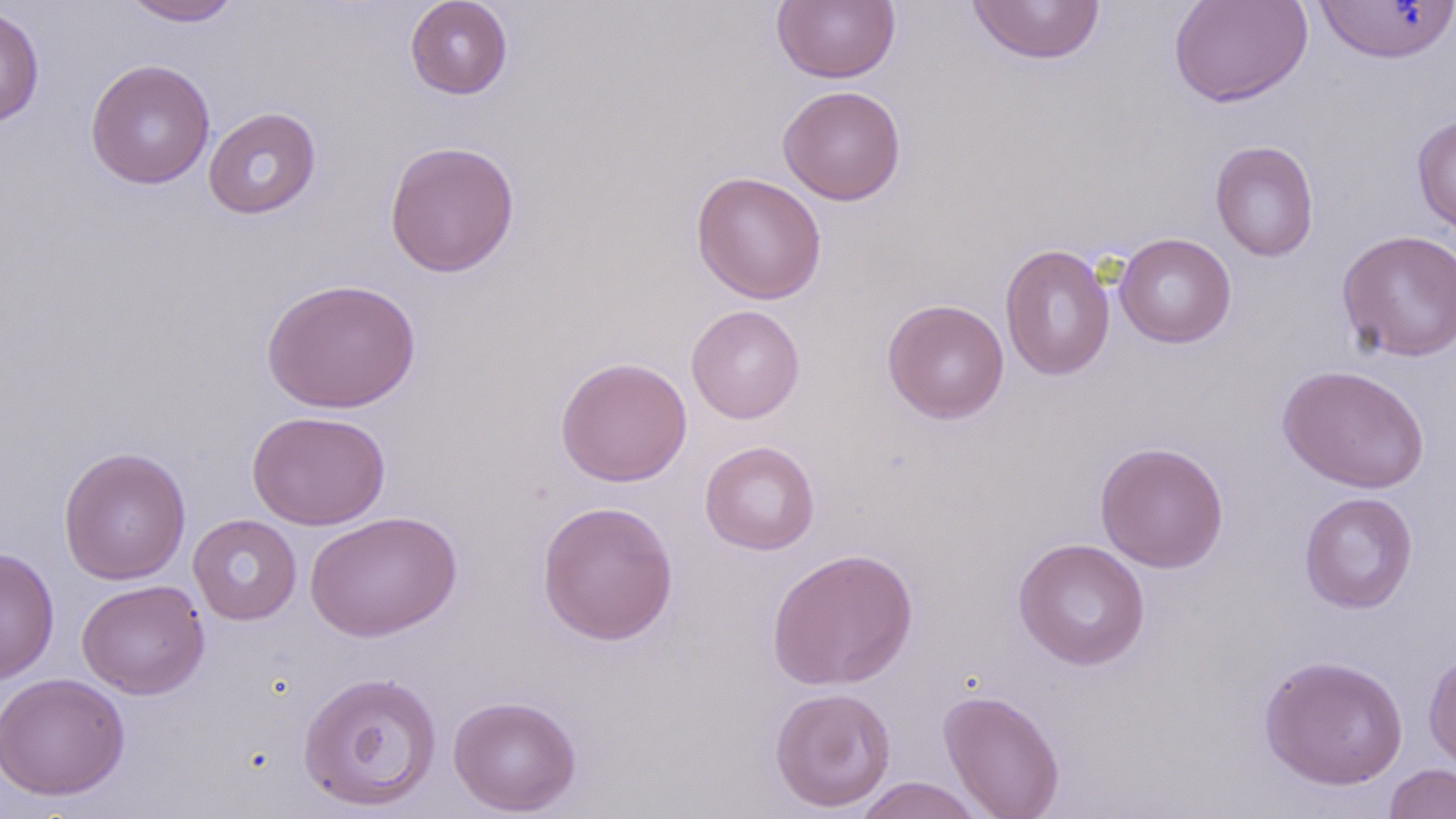 Approximate bounding boxes as (x1,y1)-(x2,y2) corner pairs in pixels. Uninfected red blood cell locations: (120,0)-(244,26), (405,0)-(513,99), (773,0)-(900,84), (1169,0)-(1312,108), (965,1)-(1106,65), (1311,1)-(1456,64), (0,6)-(45,128), (85,59)-(216,189), (778,85)-(907,205), (203,106)-(322,219), (1411,114)-(1456,238), (384,140)-(520,277), (1210,141)-(1320,262), (691,171)-(828,304), (1338,229)-(1456,362), (1115,232)-(1237,348), (999,243)-(1116,381), (261,277)-(421,413), (882,299)-(1009,423), (686,304)-(805,424), (555,356)-(693,487), (1277,364)-(1430,493), (247,410)-(390,531), (700,440)-(820,555), (1095,441)-(1229,573), (58,446)-(191,584), (1299,492)-(1419,613), (537,500)-(678,646), (304,510)-(462,642), (188,514)-(302,625), (1013,537)-(1151,670), (0,547)-(60,685), (766,547)-(918,690), (77,579)-(210,699), (1423,647)-(1456,771), (1258,654)-(1409,790), (297,670)-(443,811), (0,672)-(130,800), (769,686)-(897,813), (938,690)-(1066,819), (448,694)-(582,816), (1384,763)-(1456,818), (853,777)-(986,819). Slide-level diagnosis: negative for blood parasites. 1000x magnification. May-Grünwald-Giemsa stain. Light microscopy. Image is 1456×819 pixels. Thin blood film. One field of a larger specimen.